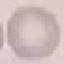
Summary:
  - Malaria status: uninfected
  - Capture: smartphone camera at the microscope eyepiece
  - Stain: Giemsa
  - Image type: cell patch, automatically extracted from a larger field of view and resized to 64 × 64 pixels
  - Preparation: thin blood smear